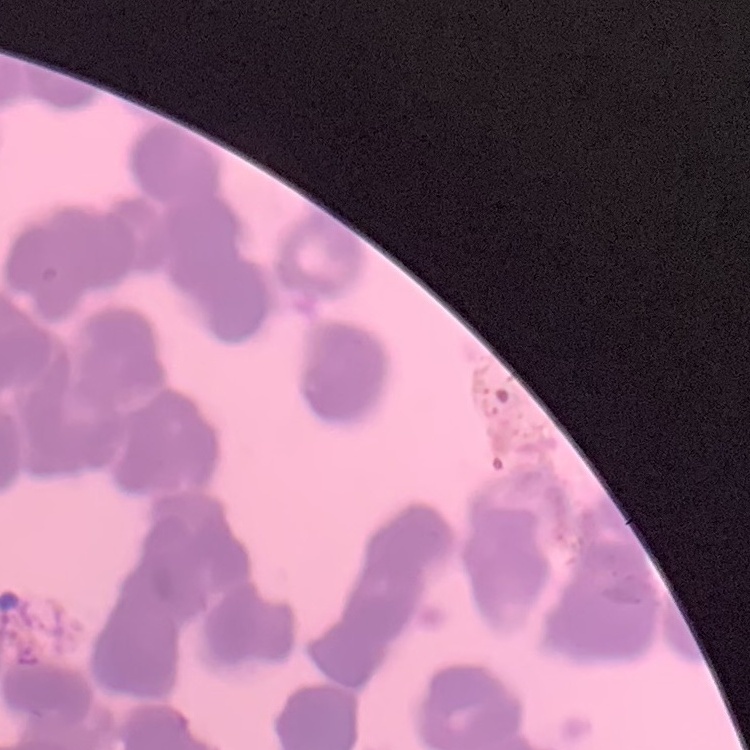
erythrocyte morphology = rouleaux formation
stain = Field's or Giemsa
image type = one tile cut from a larger photomicrograph
preparation = thin peripheral smear